Identify the cell.
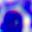

This is a leukocyte.

Summary:
  - Modality: photomicrograph
  - Magnification: 400x